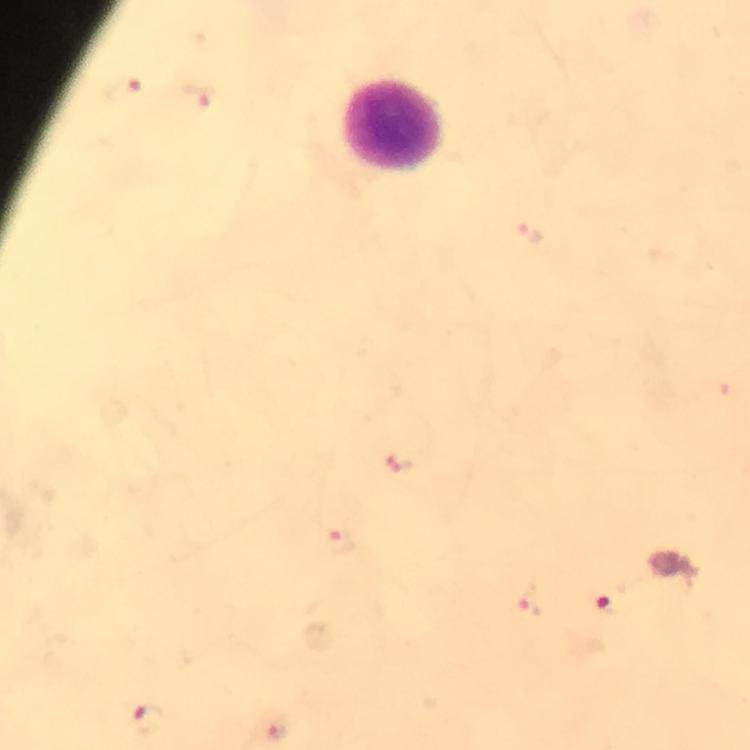

Approximate centers as [x, y] in pixels. Leukocyte locations: [394, 127]. Malaria parasite locations: [122, 92], [198, 98], [526, 234], [400, 461], [341, 541], [529, 600], [607, 604], [148, 717], [274, 732]. Giemsa-stained preparation. Immersion oil was used. From a malaria diagnostic workup. Photographed through the microscope with a smartphone camera. A crop from one field of view. Thick blood film. At 100x magnification. Image is 750×750 pixels.